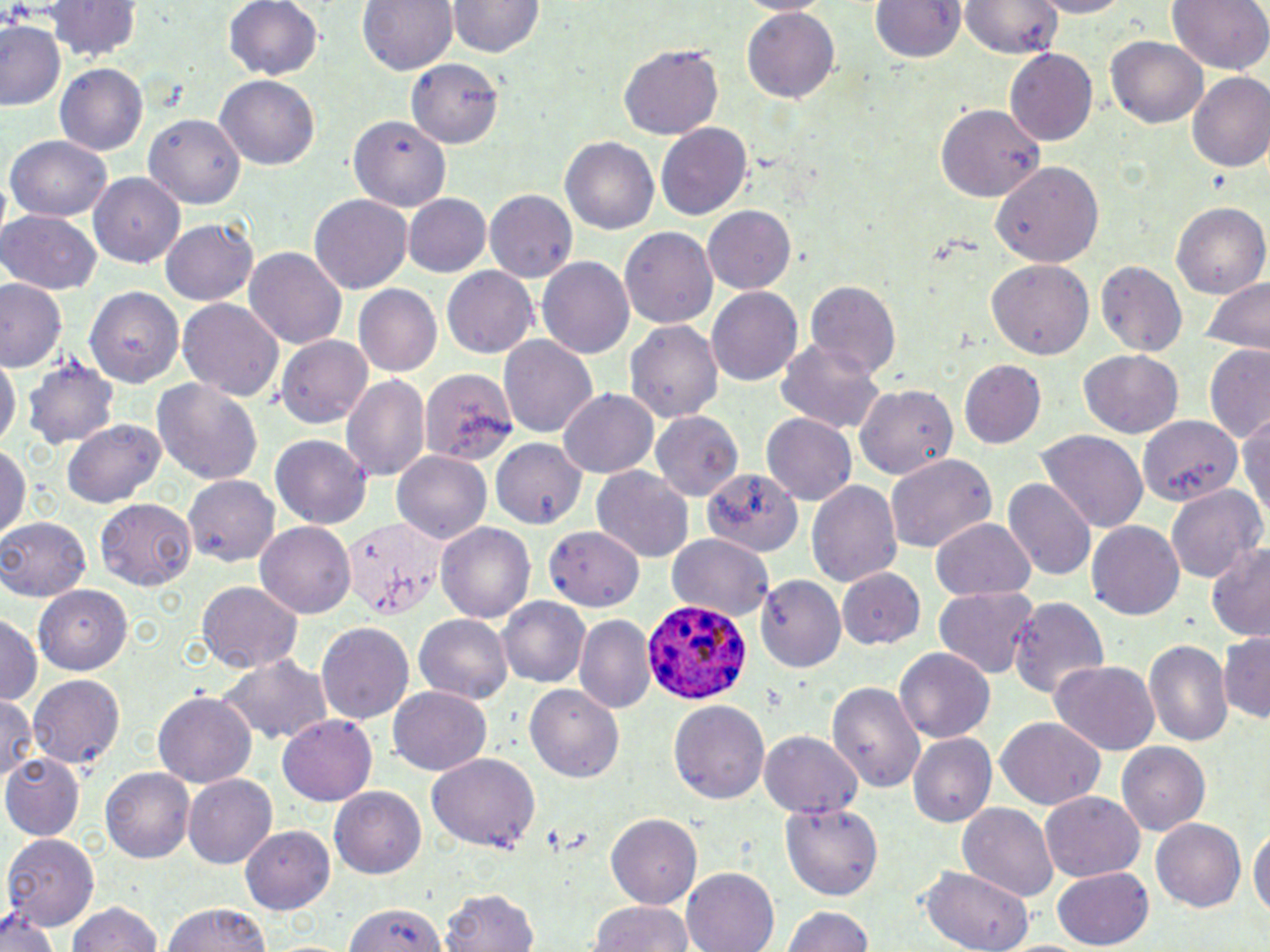
slide_level_diagnosis: Plasmodium ovale
field_of_view: one of a larger specimen
modality: light microscopy
magnification: 1000x
image_size: 1270×952 pixels
stain: May-Grünwald-Giemsa
preparation: thin blood film
uninfected_red_blood_cell_locations: 'approximate bounding boxes as named x1/y1/x2/y2 corners in pixels: (x1=43, y1=0, x2=142, y2=62), (x1=226, y1=0, x2=324, y2=82), (x1=358, y1=0, x2=457, y2=76), (x1=869, y1=0, x2=967, y2=62), (x1=957, y1=0, x2=1064, y2=58), (x1=1031, y1=0, x2=1130, y2=16), (x1=1167, y1=0, x2=1268, y2=78), (x1=450, y1=1, x2=541, y2=58), (x1=741, y1=7, x2=840, y2=104), (x1=1, y1=20, x2=66, y2=113), (x1=1106, y1=39, x2=1206, y2=127), (x1=616, y1=45, x2=724, y2=142), (x1=1005, y1=48, x2=1098, y2=145), (x1=408, y1=59, x2=502, y2=145), (x1=55, y1=62, x2=148, y2=154), (x1=1187, y1=73, x2=1270, y2=174), (x1=215, y1=75, x2=320, y2=171), (x1=935, y1=101, x2=1046, y2=201), (x1=344, y1=111, x2=451, y2=214), (x1=144, y1=112, x2=246, y2=208), (x1=655, y1=122, x2=752, y2=221), (x1=5, y1=135, x2=112, y2=221), (x1=561, y1=137, x2=658, y2=237), (x1=992, y1=160, x2=1103, y2=268), (x1=89, y1=170, x2=184, y2=268), (x1=485, y1=191, x2=578, y2=284), (x1=404, y1=194, x2=493, y2=278), (x1=309, y1=195, x2=412, y2=296), (x1=1170, y1=200, x2=1270, y2=302), (x1=703, y1=206, x2=796, y2=295), (x1=0, y1=210, x2=103, y2=294), (x1=162, y1=218, x2=258, y2=307), (x1=620, y1=226, x2=718, y2=331), (x1=245, y1=248, x2=346, y2=352), (x1=538, y1=256, x2=636, y2=359), (x1=985, y1=259, x2=1092, y2=360), (x1=1095, y1=260, x2=1186, y2=359), (x1=442, y1=266, x2=540, y2=357), (x1=1196, y1=273, x2=1269, y2=353), (x1=805, y1=280, x2=901, y2=377), (x1=0, y1=281, x2=65, y2=373), (x1=354, y1=285, x2=443, y2=376), (x1=706, y1=286, x2=803, y2=384), (x1=85, y1=288, x2=179, y2=387), (x1=177, y1=296, x2=284, y2=401), (x1=626, y1=320, x2=723, y2=425), (x1=499, y1=335, x2=597, y2=439), (x1=278, y1=336, x2=373, y2=427), (x1=774, y1=337, x2=889, y2=435), (x1=1203, y1=347, x2=1270, y2=444), (x1=0, y1=351, x2=18, y2=458), (x1=1078, y1=351, x2=1182, y2=437), (x1=25, y1=356, x2=117, y2=451), (x1=962, y1=361, x2=1046, y2=450), (x1=421, y1=365, x2=518, y2=467), (x1=342, y1=373, x2=432, y2=483), (x1=152, y1=379, x2=264, y2=485), (x1=856, y1=387, x2=957, y2=480), (x1=558, y1=388, x2=659, y2=477), (x1=1237, y1=409, x2=1270, y2=530), (x1=653, y1=412, x2=744, y2=499), (x1=1135, y1=412, x2=1246, y2=508), (x1=761, y1=415, x2=855, y2=502), (x1=64, y1=421, x2=164, y2=507), (x1=1037, y1=429, x2=1148, y2=534), (x1=270, y1=432, x2=374, y2=529), (x1=492, y1=438, x2=589, y2=528), (x1=0, y1=446, x2=28, y2=541), (x1=391, y1=450, x2=491, y2=545), (x1=885, y1=452, x2=997, y2=555), (x1=590, y1=469, x2=694, y2=564), (x1=704, y1=470, x2=803, y2=559), (x1=182, y1=476, x2=280, y2=563), (x1=1002, y1=476, x2=1097, y2=583), (x1=806, y1=478, x2=904, y2=591), (x1=1167, y1=483, x2=1265, y2=586), (x1=98, y1=498, x2=198, y2=590), (x1=1086, y1=517, x2=1184, y2=617), (x1=2, y1=518, x2=91, y2=603), (x1=929, y1=519, x2=1037, y2=599), (x1=436, y1=520, x2=535, y2=622), (x1=255, y1=522, x2=357, y2=618), (x1=544, y1=526, x2=642, y2=611), (x1=667, y1=534, x2=775, y2=622), (x1=1206, y1=542, x2=1270, y2=640), (x1=839, y1=568, x2=924, y2=649), (x1=756, y1=573, x2=844, y2=673), (x1=196, y1=580, x2=303, y2=675), (x1=933, y1=585, x2=1040, y2=682), (x1=34, y1=587, x2=132, y2=673), (x1=1008, y1=596, x2=1110, y2=702), (x1=498, y1=597, x2=592, y2=691), (x1=0, y1=614, x2=40, y2=707), (x1=575, y1=614, x2=655, y2=715), (x1=415, y1=615, x2=513, y2=702), (x1=319, y1=621, x2=415, y2=724), (x1=1219, y1=633, x2=1269, y2=723), (x1=1144, y1=638, x2=1232, y2=749), (x1=897, y1=648, x2=995, y2=742), (x1=217, y1=653, x2=333, y2=748), (x1=1051, y1=661, x2=1160, y2=757), (x1=28, y1=675, x2=124, y2=773), (x1=829, y1=680, x2=924, y2=794), (x1=524, y1=682, x2=626, y2=782), (x1=388, y1=684, x2=490, y2=776), (x1=153, y1=691, x2=256, y2=789), (x1=0, y1=692, x2=36, y2=785), (x1=670, y1=700, x2=769, y2=803), (x1=278, y1=715, x2=376, y2=806), (x1=995, y1=718, x2=1107, y2=810), (x1=759, y1=732, x2=862, y2=818), (x1=908, y1=732, x2=997, y2=827), (x1=1117, y1=742, x2=1212, y2=837), (x1=426, y1=753, x2=540, y2=852), (x1=2, y1=754, x2=83, y2=841), (x1=102, y1=766, x2=194, y2=864), (x1=183, y1=774, x2=276, y2=869), (x1=330, y1=786, x2=428, y2=879), (x1=1039, y1=793, x2=1144, y2=883), (x1=781, y1=800, x2=884, y2=901), (x1=958, y1=803, x2=1058, y2=902), (x1=609, y1=812, x2=703, y2=907), (x1=1151, y1=818, x2=1247, y2=915), (x1=1249, y1=824, x2=1269, y2=924), (x1=240, y1=825, x2=337, y2=911), (x1=4, y1=833, x2=100, y2=931), (x1=681, y1=866, x2=780, y2=952), (x1=919, y1=866, x2=1033, y2=951), (x1=1052, y1=868, x2=1153, y2=948), (x1=438, y1=888, x2=538, y2=952), (x1=343, y1=899, x2=443, y2=951), (x1=587, y1=899, x2=697, y2=952), (x1=66, y1=901, x2=164, y2=952), (x1=162, y1=901, x2=275, y2=952), (x1=781, y1=903, x2=878, y2=952), (x1=0, y1=905, x2=61, y2=952)'
plasmodium_ovale_infected_red_blood_cell_locations: 'approximate bounding boxes as named x1/y1/x2/y2 corners in pixels: (x1=643, y1=595, x2=756, y2=707)'